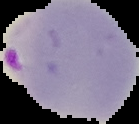

image type = segmented cell region on a black background
preparation = thin blood smear
malaria status = parasitized
image size = 139×124 pixels